Report the malaria status of this cell.
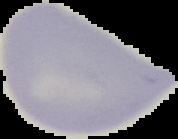
It is uninfected.

From a thin blood smear. Segmented cell region on a black background. Image is 178×139 pixels.